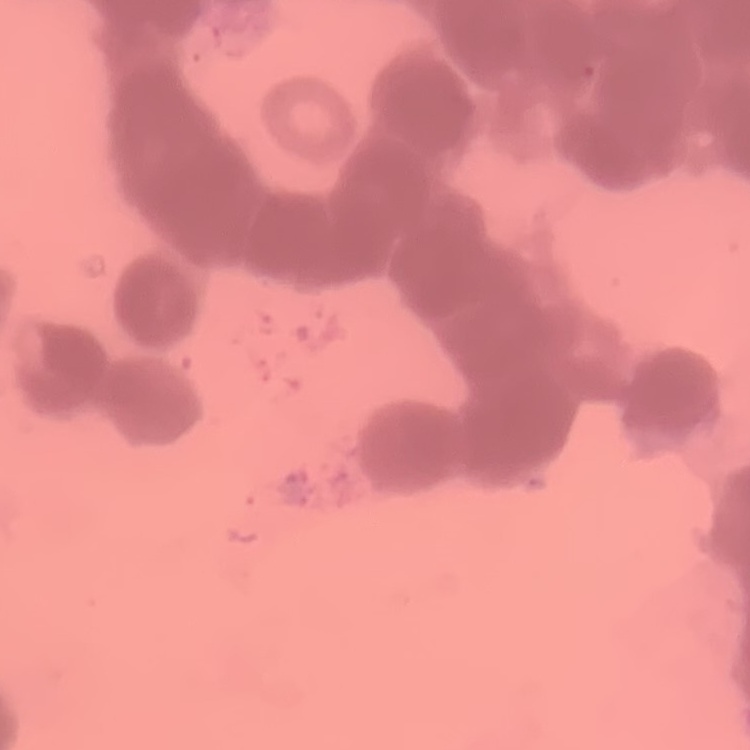
Summary:
  - Red blood cell morphology: rouleaux formation
  - Preparation: thin blood film
  - Stain: Field's or Giemsa
  - Image type: one tile cut from a larger photomicrograph